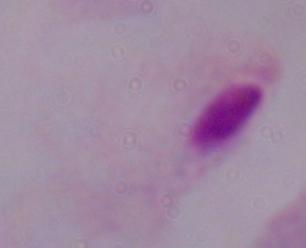
{
  "modality": "micrograph",
  "magnification": "1000x",
  "identification": "trichomonad"
}